Classify this cell by malaria status.
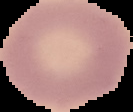

Uninfected.

From a thin blood film. Image is 133×112 pixels. Cell region segmented out of the field of view; the surrounding area is masked to black.